Assess this cell for malaria.
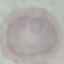

Uninfected.

image_type: automatically extracted cell patch, resized to 64 × 64 pixels
stain: Giemsa
preparation: thin smear
capture: smartphone through the microscope eyepiece